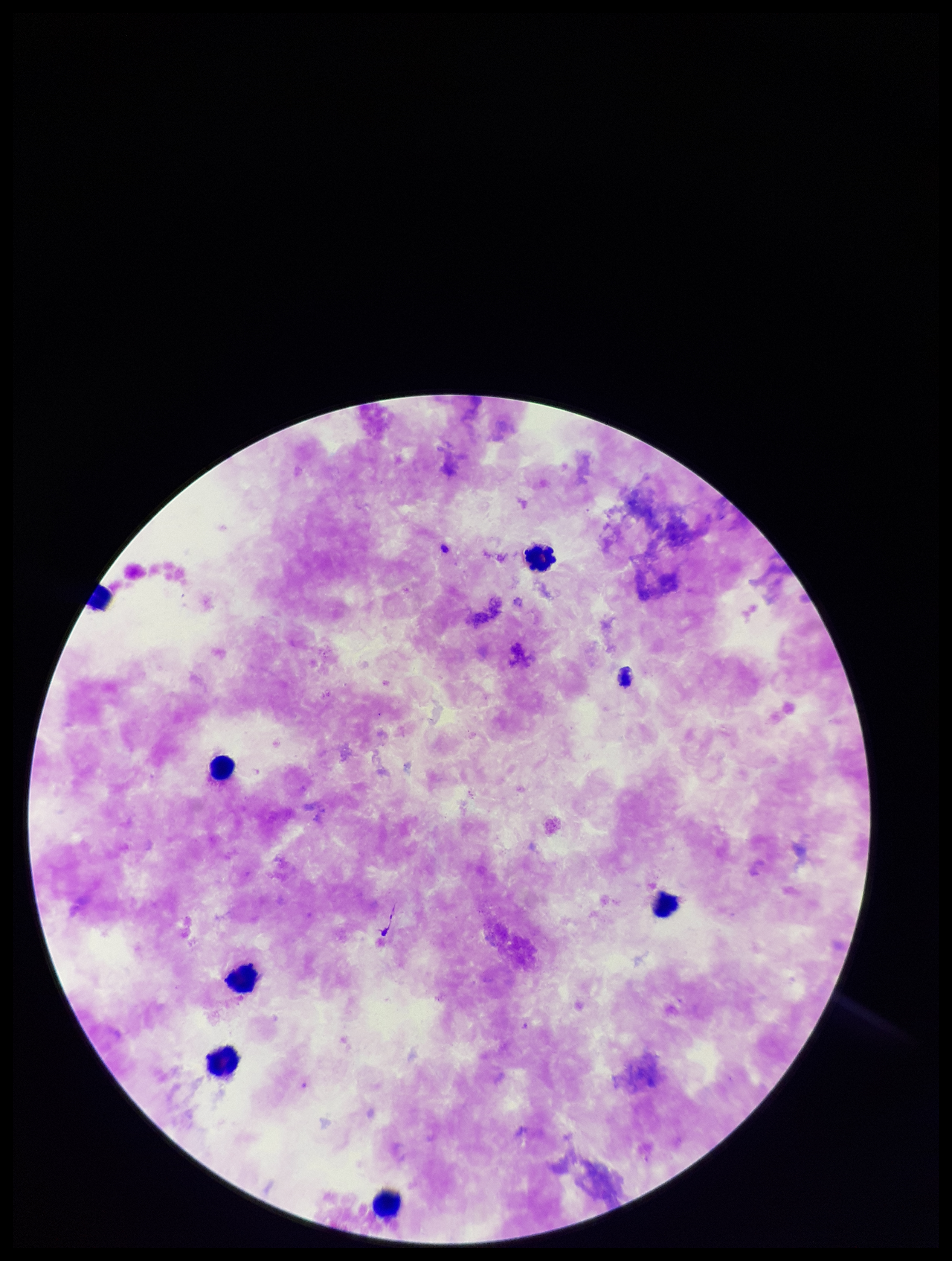 Plasmodium parasites: none identified. Preparation: thick. Image is 952×1261 pixels. Parasite count: 0. Leukocyte count: 7. Single field of view. Photographed through the microscope eyepiece with a smartphone camera. Patient malaria status: negative. Stained with Giemsa.